State the preparation type.
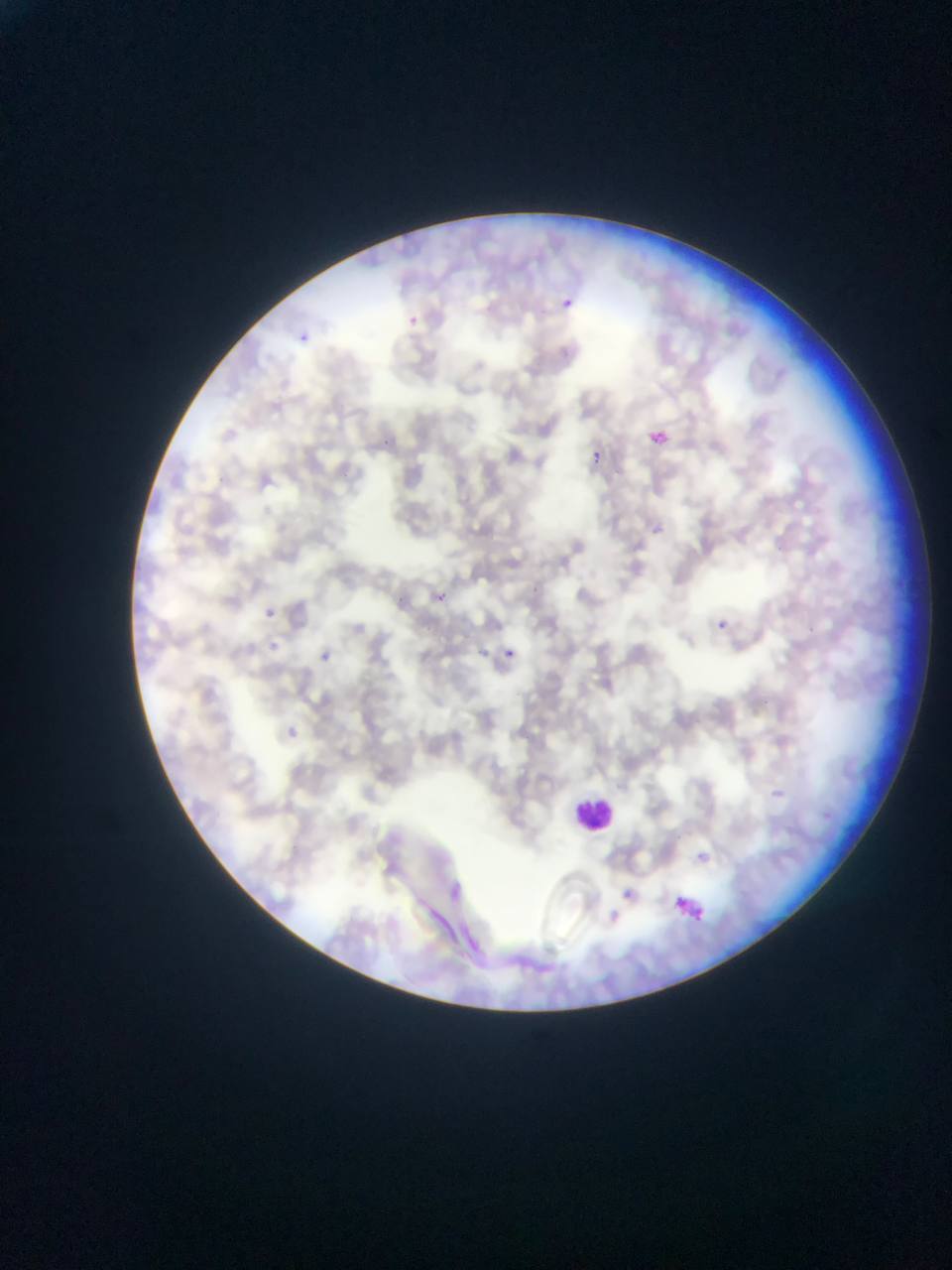

Thin blood film.

Approximate bounding boxes as [left, top, right, bottom] in pixels. Malaria parasite locations: [559, 291, 579, 304], [403, 311, 428, 329], [299, 332, 310, 342], [646, 418, 684, 459], [583, 443, 604, 460], [653, 516, 688, 556], [253, 592, 271, 612], [436, 593, 447, 603], [718, 621, 729, 630], [261, 635, 282, 653], [316, 642, 364, 670], [474, 643, 486, 660], [506, 649, 515, 657], [286, 721, 316, 739], [769, 782, 786, 815], [689, 837, 719, 862], [445, 873, 481, 916], [613, 875, 638, 893], [674, 876, 707, 906], [693, 910, 703, 921], [603, 913, 628, 930]. Leukocyte locations: [574, 777, 617, 835]. Image is 952×1270 pixels. Mobile-phone photograph taken through the microscope. Sample from Ghana. One field of view.